Identify the parasite.
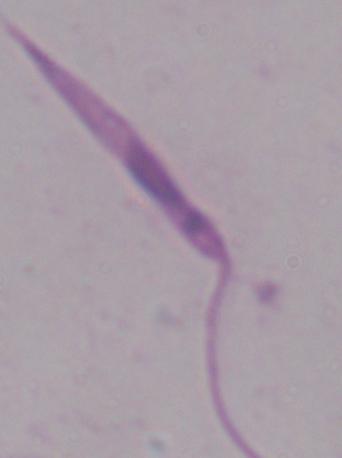
This is Leishmania.

Photomicrograph. 1000x magnification.